Classify this cell by malaria status.
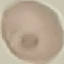

It is uninfected.

preparation: thin blood film
stain: Giemsa
image_type: cell patch, automatically extracted from a larger field of view and resized to 64 × 64 pixels
capture: smartphone through the microscope eyepiece